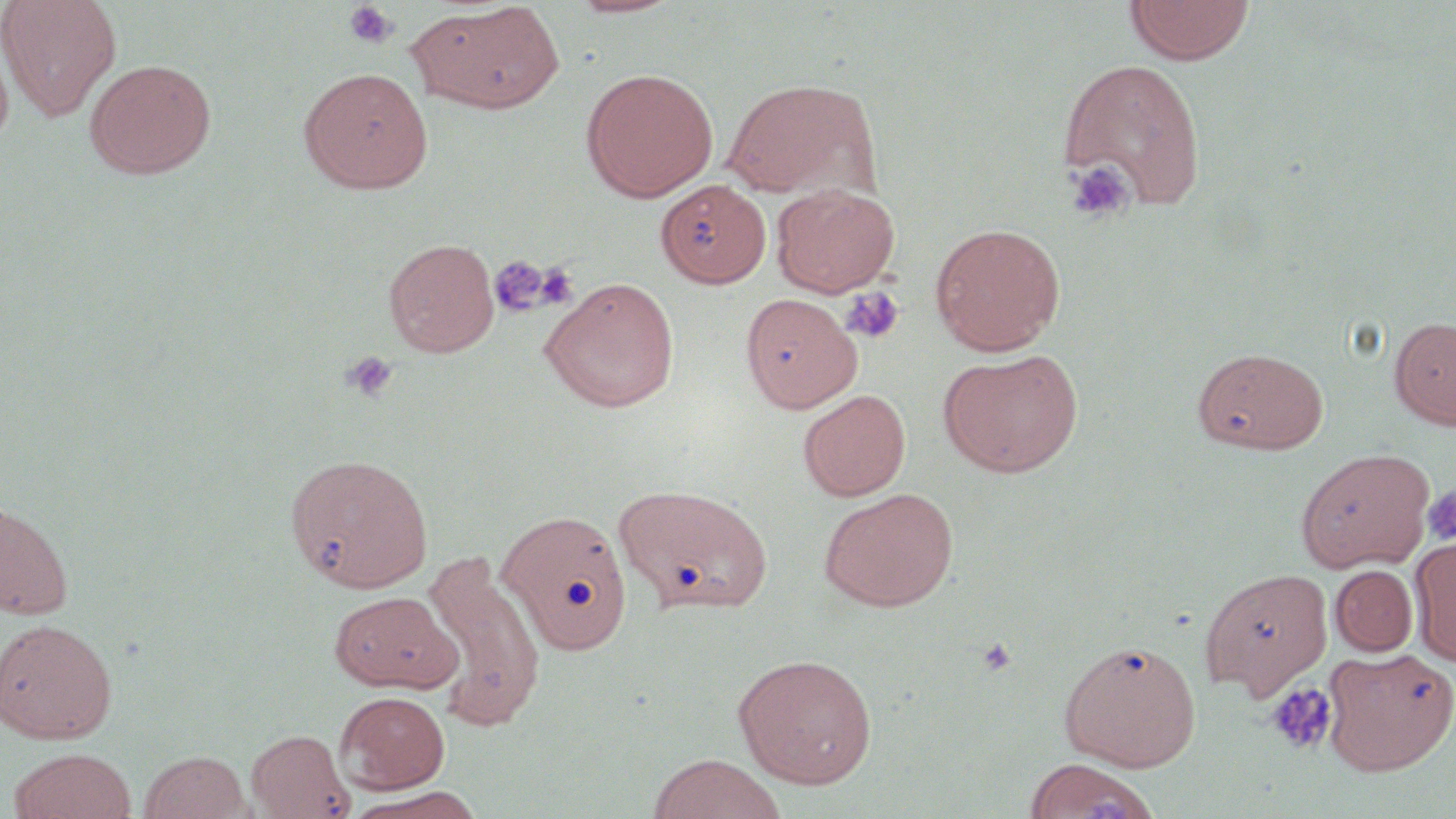

Summary:
  - Coordinate format: approximate bounding boxes as (x1, y1, x2, y2) in pixels
  - Uninfected red blood cell locations: (0, 0, 121, 122), (563, 0, 686, 19), (1124, 0, 1254, 65), (407, 3, 564, 114), (0, 37, 14, 154), (1057, 57, 1207, 210), (85, 59, 216, 179), (298, 67, 433, 194), (581, 67, 718, 202), (722, 77, 878, 199), (657, 179, 770, 288), (770, 183, 900, 298), (930, 222, 1066, 355), (384, 238, 499, 357), (540, 276, 680, 412), (740, 293, 861, 413), (1389, 315, 1456, 430), (1193, 346, 1329, 454), (938, 350, 1083, 477), (798, 389, 911, 501), (1295, 447, 1435, 572), (284, 452, 434, 594), (616, 484, 772, 616), (819, 487, 958, 612), (1, 500, 74, 621), (498, 509, 632, 656), (1410, 537, 1456, 667), (423, 553, 548, 732), (1330, 565, 1418, 657), (1200, 567, 1333, 699), (329, 591, 460, 693), (0, 618, 118, 744), (1059, 638, 1201, 771), (1322, 645, 1456, 775), (732, 653, 877, 789), (336, 691, 450, 793), (247, 728, 355, 818), (7, 747, 137, 819), (139, 750, 251, 819), (645, 754, 789, 819), (1025, 758, 1159, 819), (343, 787, 488, 819)
  - Platelet locations: (343, 1, 400, 48), (1064, 159, 1134, 224), (489, 254, 551, 317), (535, 263, 578, 310), (840, 287, 905, 344), (341, 350, 399, 402), (1422, 485, 1456, 545), (976, 636, 1017, 677), (1265, 682, 1337, 755), (1089, 793, 1131, 819)
  - Slide-level diagnosis: no evidence of blood parasites
  - Stain: May-Grünwald-Giemsa
  - Preparation: thin blood film
  - Modality: optical microscopy
  - Image size: 1456×819 pixels
  - Magnification: 1000x
  - Field of view: single